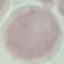 Malaria status: uninfected. Thin blood film. Photographed with a smartphone camera at the microscope eyepiece. Giemsa-stained preparation. Automatically extracted cell patch, resized to 64 × 64 pixels.